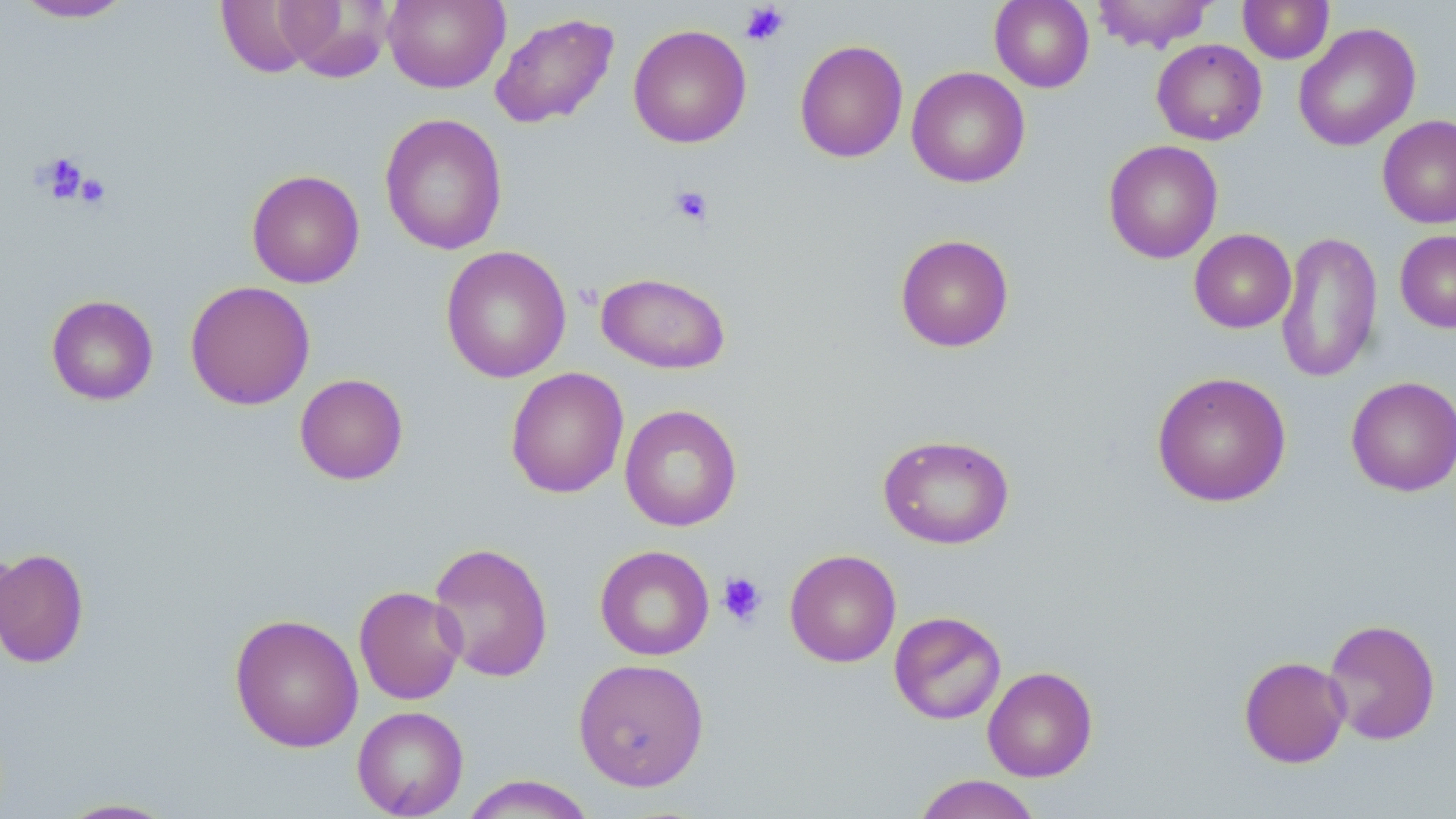

{
  "slide_level_diagnosis": "negative for blood parasites",
  "preparation": "thin blood smear",
  "platelet_locations": "approximate bounding boxes as [x1, y1, x2, y2] in pixels: [739, 3, 790, 46], [36, 152, 90, 203], [76, 173, 111, 209], [669, 185, 714, 226], [717, 572, 768, 627]",
  "uninfected_red_blood_cell_locations": "approximate bounding boxes as [x1, y1, x2, y2] in pixels: [214, 0, 323, 78], [383, 0, 509, 93], [989, 0, 1094, 92], [1091, 0, 1217, 53], [1237, 0, 1334, 64], [11, 1, 136, 23], [273, 1, 393, 82], [490, 12, 619, 129], [1293, 23, 1421, 151], [628, 24, 751, 148], [794, 39, 909, 163], [1152, 39, 1267, 145], [906, 66, 1030, 188], [379, 113, 508, 256], [1377, 115, 1456, 229], [1103, 139, 1223, 264], [246, 169, 365, 288], [1189, 229, 1296, 333], [1275, 230, 1383, 383], [1395, 230, 1456, 333], [895, 233, 1014, 352], [440, 245, 572, 383], [596, 272, 731, 375], [185, 280, 315, 410], [46, 294, 159, 406], [505, 367, 629, 498], [1151, 371, 1292, 507], [294, 373, 409, 485], [1346, 376, 1456, 496], [620, 404, 742, 532], [877, 433, 1014, 549], [428, 541, 554, 683], [0, 542, 20, 659], [594, 545, 714, 661], [0, 547, 90, 669], [785, 549, 901, 667], [353, 585, 467, 705], [889, 611, 1007, 725], [229, 613, 363, 753], [1323, 618, 1441, 745], [1238, 655, 1350, 768], [572, 658, 710, 792], [982, 665, 1098, 782], [352, 706, 469, 818], [911, 774, 1043, 819], [460, 775, 598, 818], [55, 797, 179, 818]",
  "modality": "optical microscopy",
  "field_of_view": "one of a larger specimen",
  "magnification": "1000x",
  "stain": "May-Grünwald-Giemsa",
  "image_size": "1456×819 pixels"
}